Assess the morphology of the red blood cells.
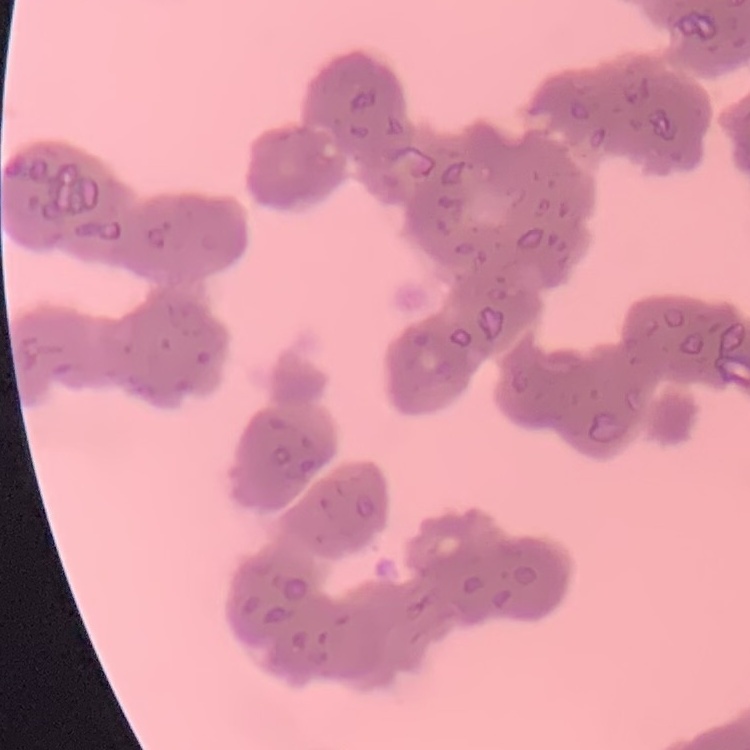
Rouleaux formation.

Summary:
  - Image type: square crop of a larger photomicrograph
  - Stain: Field's or Giemsa
  - Preparation: thin blood smear